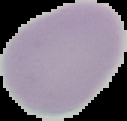

Image is 127×121 pixels. The area outside the segmented cell region is set to black. Result: no malaria parasites seen. From a thin blood film.